Report the malaria status.
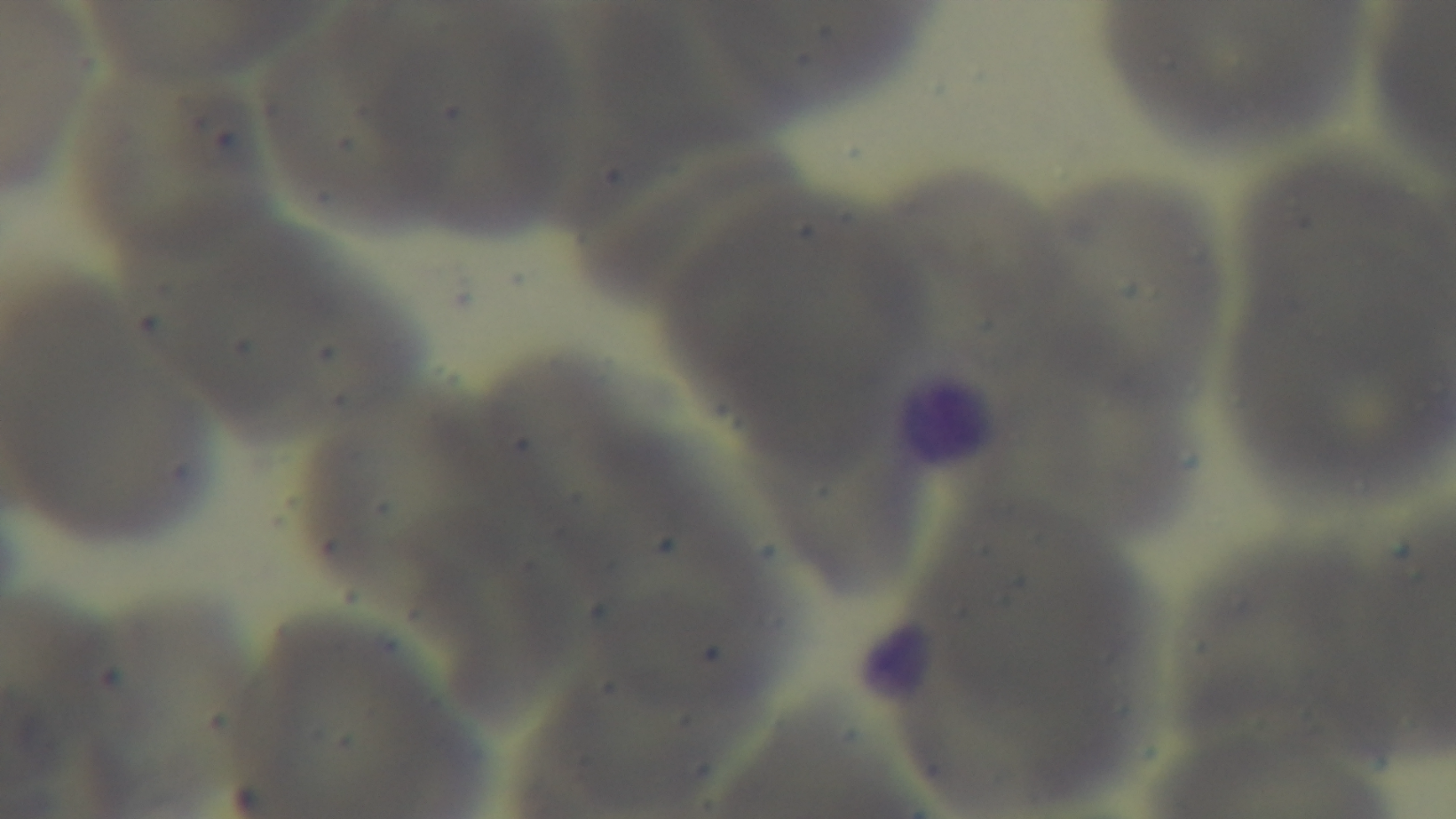

Uninfected.

Summary:
  - Preparation: thin smear
  - Modality: light microscopy
  - Stain: Giemsa
  - Objective: 100x oil immersion
  - Field of view: one from the slide
  - Capture: mounted 4K digital camera